Outline each blood parasite and name the species.
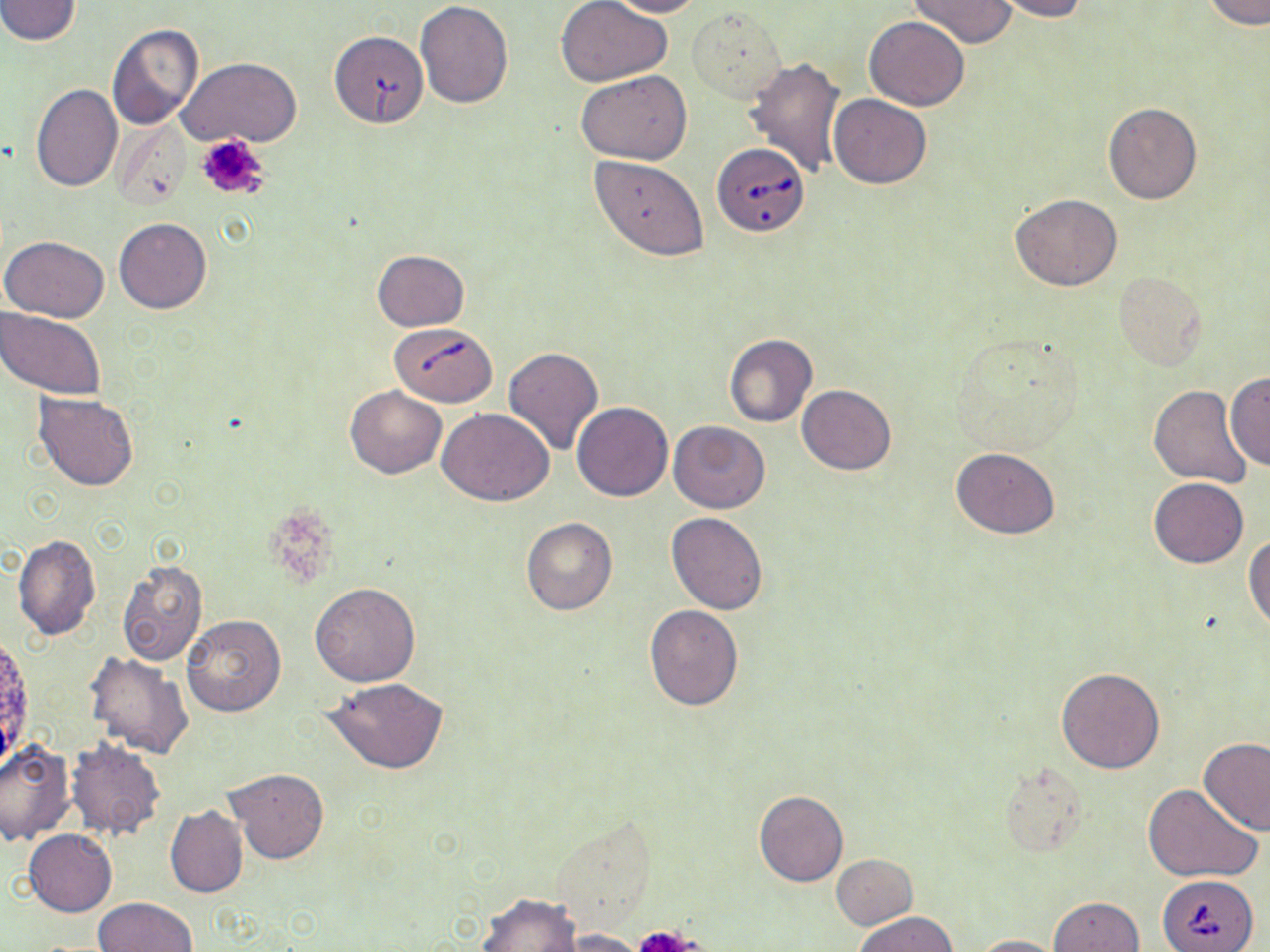
Approximate bounding boxes as (x1,y1)-(x2,y2) corner pairs in pixels.
Babesia divergens-infected red blood cells: (332,33)-(428,130), (711,141)-(810,233), (389,323)-(498,407), (1159,875)-(1258,951).
No Plasmodium falciparum, Plasmodium ovale, Plasmodium malariae, Plasmodium vivax, or Trypanosoma brucei observed.

slide-level diagnosis = Babesia divergens
platelet locations = approximate bounding boxes as (x1,y1)-(x2,y2) corner pairs in pixels: (195,134)-(271,201), (637,923)-(702,951)
uninfected red blood cell locations = approximate bounding boxes as (x1,y1)-(x2,y2) corner pairs in pixels: (0,0)-(82,45), (557,0)-(671,86), (604,0)-(705,18), (991,0)-(1088,21), (1205,0)-(1269,30), (415,1)-(514,107), (908,1)-(1017,48), (688,7)-(786,103), (864,16)-(969,110), (106,23)-(204,129), (744,56)-(849,178), (177,57)-(301,147), (576,70)-(690,163), (30,83)-(122,192), (829,93)-(931,188), (1104,102)-(1201,204), (591,156)-(708,261), (1010,193)-(1122,291), (114,217)-(212,314), (1,235)-(110,323), (372,249)-(469,331), (1113,271)-(1207,370), (0,307)-(108,401), (948,331)-(1087,454), (724,333)-(817,427), (501,347)-(603,456), (1225,372)-(1269,473), (798,384)-(896,474), (344,385)-(447,479), (1149,385)-(1252,487), (34,393)-(139,490), (572,402)-(673,501), (437,408)-(554,505), (667,421)-(772,514), (950,447)-(1060,539), (1148,477)-(1248,568), (666,512)-(770,614), (521,518)-(617,615), (1244,533)-(1270,632), (14,534)-(100,641), (116,558)-(207,667), (311,582)-(420,686), (645,605)-(743,711), (179,614)-(286,717), (85,653)-(195,758), (1055,667)-(1166,773), (324,677)-(449,775), (1198,737)-(1270,836), (1,739)-(75,845), (65,740)-(166,840), (998,762)-(1087,855), (224,767)-(329,865), (1144,785)-(1261,883), (754,790)-(847,887), (166,805)-(249,899), (22,829)-(115,917), (832,854)-(918,929), (477,892)-(582,952), (1047,897)-(1144,952), (93,898)-(197,951), (855,911)-(958,951), (550,928)-(652,951), (973,934)-(1064,952)
stain = May-Grünwald-Giemsa
preparation = thin blood film
field of view = single
modality = light microscopy
image size = 1270×952 pixels
magnification = 1000x